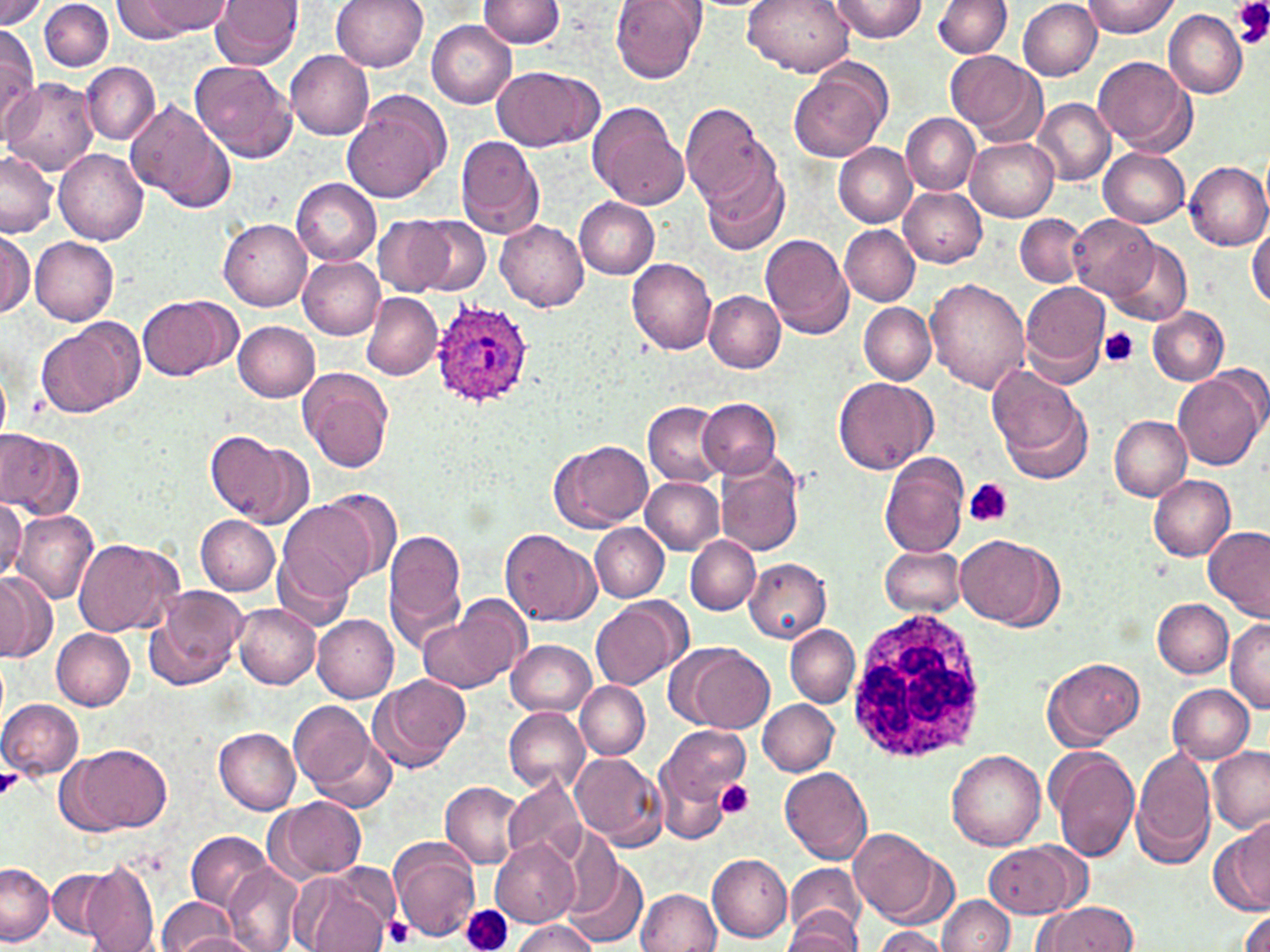

slide-level diagnosis = Plasmodium ovale
stain = May-Grünwald-Giemsa
field of view = single
preparation = thin blood smear
image size = 1270×952 pixels
platelet locations = approximate bounding boxes as [x1, y1, x2, y2] in pixels: [1231, 0, 1270, 48], [1100, 329, 1139, 366], [964, 477, 1013, 528], [0, 766, 25, 801], [715, 779, 755, 820], [461, 905, 514, 952], [385, 916, 416, 947]
white blood cell locations = approximate bounding boxes as [x1, y1, x2, y2] in pixels: [843, 604, 992, 766]
modality = light microscopy
uninfected red blood cell locations = approximate bounding boxes as [x1, y1, x2, y2] in pixels: [0, 0, 49, 30], [40, 0, 113, 72], [114, 0, 201, 40], [210, 0, 304, 69], [332, 0, 428, 72], [479, 0, 564, 48], [612, 0, 706, 83], [744, 0, 855, 77], [828, 0, 928, 42], [1081, 0, 1177, 36], [933, 1, 1011, 59], [1017, 1, 1100, 79], [1163, 10, 1247, 98], [426, 20, 516, 108], [0, 25, 38, 127], [284, 49, 373, 139], [944, 50, 1046, 147], [1092, 56, 1196, 155], [189, 60, 297, 164], [789, 61, 892, 161], [81, 62, 160, 144], [491, 64, 602, 151], [4, 78, 99, 176], [342, 92, 451, 204], [1034, 98, 1114, 184], [124, 99, 237, 212], [586, 100, 690, 210], [679, 101, 771, 208], [900, 113, 980, 195], [454, 135, 545, 239], [965, 137, 1059, 222], [833, 144, 917, 226], [1098, 147, 1191, 229], [55, 148, 149, 244], [700, 150, 788, 257], [0, 151, 57, 238], [1185, 161, 1270, 250], [292, 178, 381, 266], [899, 187, 986, 267], [864, 191, 974, 322], [574, 197, 659, 279], [1067, 213, 1161, 303], [1016, 214, 1088, 288], [374, 217, 456, 297], [415, 217, 491, 294], [217, 218, 312, 310], [496, 219, 590, 310], [1247, 223, 1269, 312], [839, 225, 919, 305], [1, 228, 33, 318], [760, 234, 854, 340], [29, 238, 119, 325], [1105, 240, 1193, 326], [297, 255, 384, 339], [628, 258, 717, 355], [925, 279, 1028, 396], [1020, 283, 1111, 386], [704, 291, 785, 372], [362, 293, 442, 379], [136, 296, 238, 381], [859, 303, 936, 384], [1146, 305, 1228, 385], [35, 318, 144, 421], [232, 320, 319, 402], [1173, 366, 1267, 471], [300, 367, 394, 473], [989, 367, 1093, 483], [834, 375, 934, 474], [697, 397, 781, 479], [644, 403, 725, 487], [1107, 414, 1191, 501], [0, 428, 84, 521], [209, 432, 309, 528], [551, 439, 653, 531], [879, 452, 971, 558], [715, 453, 805, 556], [1148, 476, 1236, 561], [641, 477, 725, 553], [318, 489, 403, 583], [0, 498, 26, 586], [275, 498, 377, 607], [12, 509, 99, 606], [195, 516, 279, 595], [590, 523, 669, 602], [383, 526, 467, 645], [1203, 527, 1270, 621], [500, 528, 600, 626], [954, 534, 1060, 628], [685, 536, 760, 614], [72, 538, 184, 637], [880, 545, 966, 616], [688, 546, 825, 629], [745, 559, 831, 642], [273, 560, 352, 628], [0, 570, 55, 661], [148, 586, 250, 690], [415, 596, 528, 696], [590, 598, 689, 691], [1153, 599, 1233, 678], [233, 603, 321, 688], [313, 616, 399, 702], [1226, 617, 1270, 713], [786, 624, 860, 706], [52, 629, 134, 709], [506, 639, 596, 717], [677, 645, 775, 734], [1042, 656, 1145, 749], [370, 673, 471, 772], [576, 680, 650, 759], [1168, 683, 1255, 764], [0, 697, 84, 780], [287, 697, 390, 805], [757, 699, 839, 775], [503, 707, 589, 792], [657, 725, 749, 811], [214, 728, 302, 814], [59, 743, 173, 836], [1131, 744, 1217, 870], [1206, 745, 1270, 831], [1046, 747, 1139, 862], [946, 748, 1046, 852], [570, 752, 666, 848], [655, 766, 731, 845], [780, 767, 874, 866], [502, 773, 589, 868], [441, 781, 526, 868], [268, 796, 367, 881], [1210, 818, 1270, 919], [850, 827, 946, 926], [186, 831, 274, 911], [388, 840, 481, 942], [491, 840, 578, 926], [986, 841, 1084, 917], [707, 853, 792, 943], [564, 857, 647, 947], [80, 860, 161, 952], [222, 862, 303, 952], [1, 863, 55, 944], [46, 867, 125, 942], [783, 867, 865, 950], [294, 870, 390, 952], [636, 889, 722, 952], [938, 894, 1015, 952], [154, 897, 242, 950], [371, 900, 422, 950], [1034, 901, 1141, 952], [1236, 909, 1270, 952], [784, 914, 861, 951], [509, 920, 601, 952], [870, 926, 949, 952], [168, 932, 258, 951]
magnification = 1000x
Plasmodium ovale-infected red blood cell locations = approximate bounding boxes as [x1, y1, x2, y2] in pixels: [428, 301, 536, 409]